State which parasite is depicted.
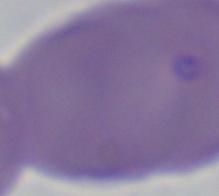
Babesia.

{
  "modality": "micrograph",
  "magnification": "1000x"
}